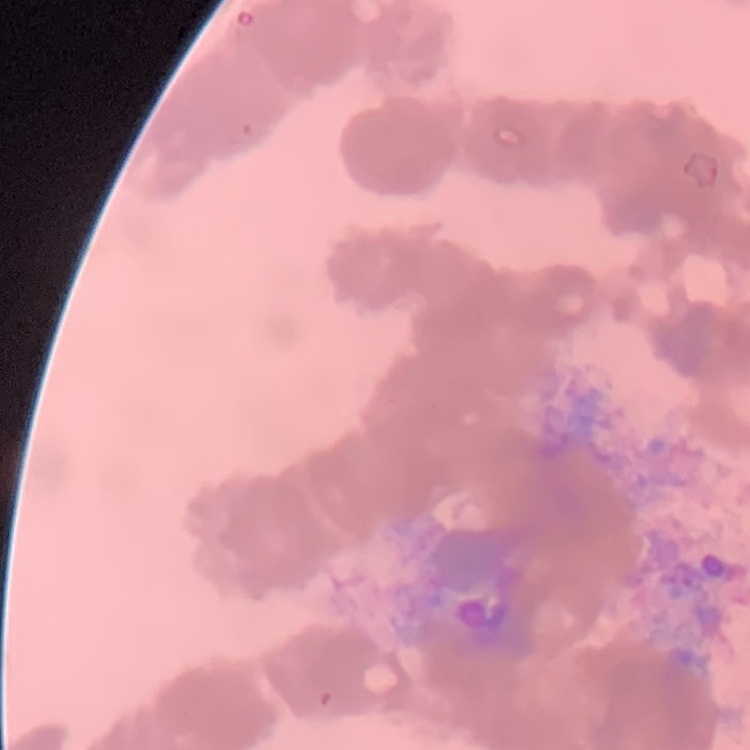
The erythrocytes exhibit rouleaux formation. Thin blood smear. One tile cut from a larger photomicrograph. Stained with either Field's or Giemsa.